Identify the preparation type.
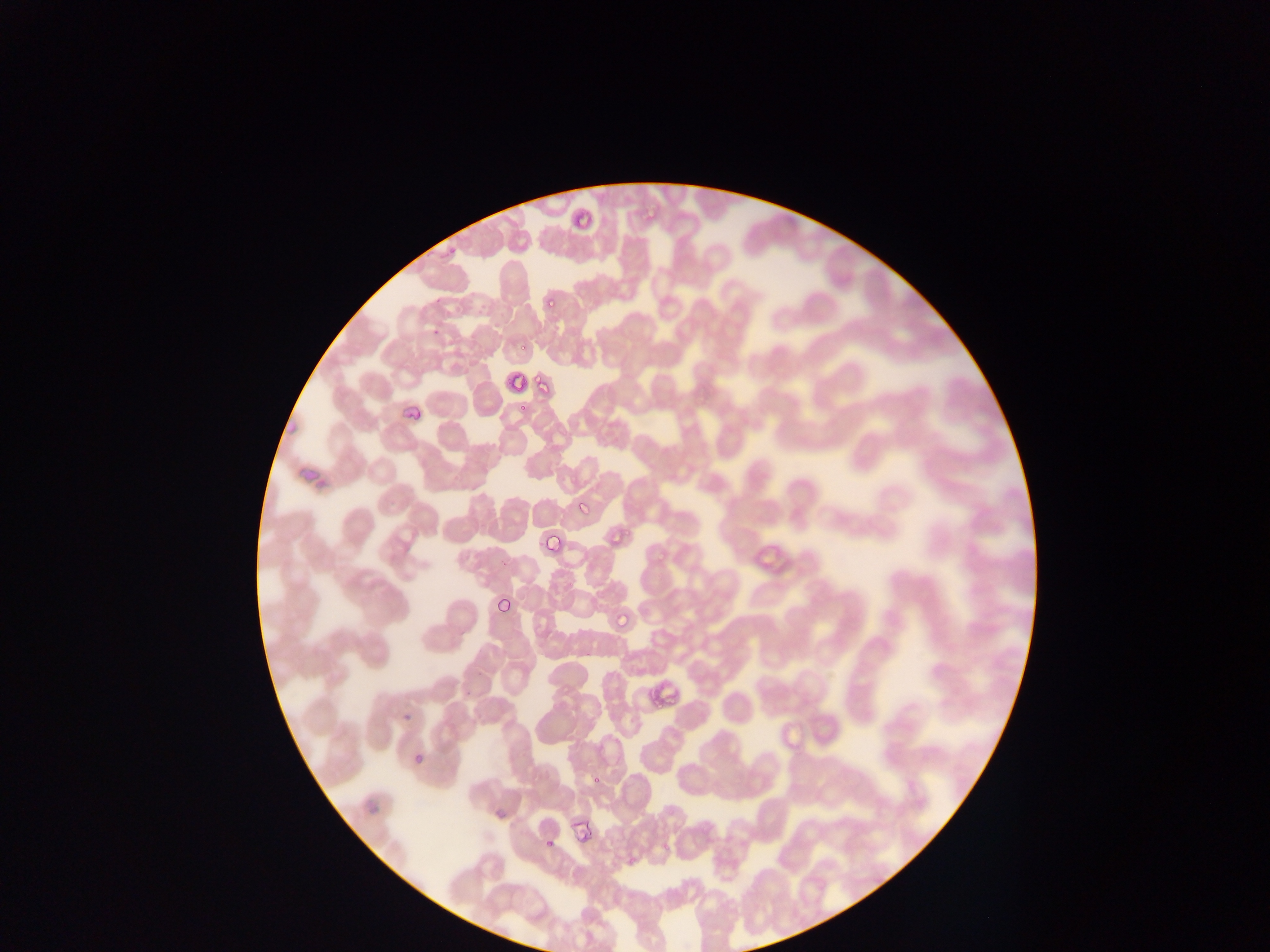
This is a thin smear.

Approximate bounding boxes as (left, top, right, bottom) in pixels. Plasmodium parasite locations: (569, 208, 600, 236), (544, 295, 561, 314), (517, 340, 530, 354), (504, 369, 531, 398), (535, 376, 552, 391), (517, 403, 532, 412), (577, 502, 592, 516), (612, 524, 631, 536), (537, 528, 571, 562), (496, 598, 510, 615), (615, 602, 643, 629), (410, 755, 424, 764), (592, 772, 605, 786), (544, 835, 555, 849). Image is 1270×952 pixels. One field of view. Photographed through a microscope with a mobile-phone camera. Sample from Ghana.